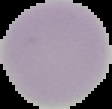
{
  "result": "no malaria parasites seen",
  "image_size": "112×109 pixels",
  "preparation": "thin blood film",
  "image_type": "segmented cell region on a black background"
}